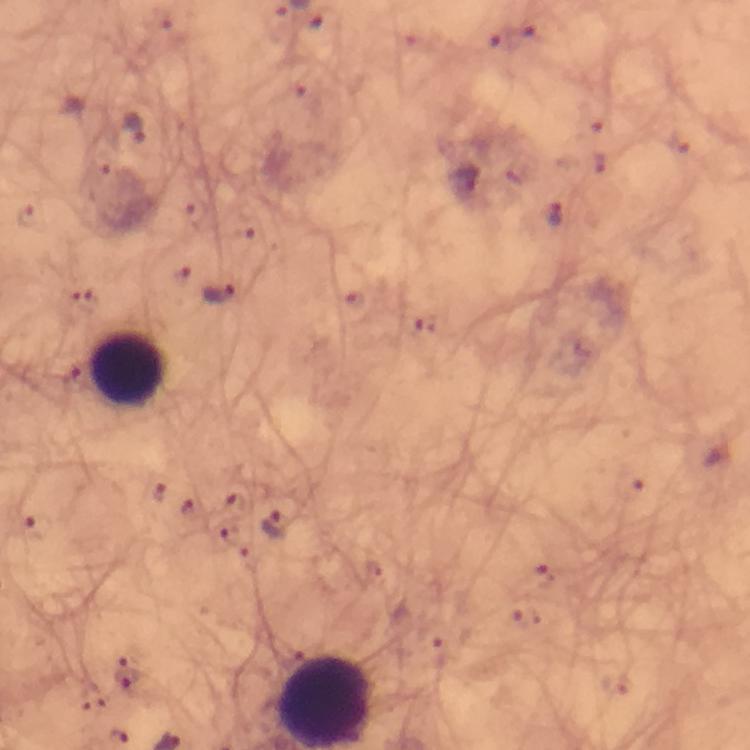

{
  "magnification": "100x",
  "stain": "Giemsa",
  "context": "from a diagnostic examination for malaria",
  "image_size": "750×750 pixels",
  "immersion_oil": "applied",
  "plasmodium_parasite_locations": "approximate centers as {x, y} in pixels: {133, 127}, {463, 180}, {556, 215}, {218, 292}, {274, 525}, {129, 675}",
  "preparation": "thick blood smear",
  "capture": "smartphone mounted on the microscope",
  "leukocyte_locations": "approximate centers as {x, y} in pixels: {128, 369}",
  "cropped_from": "a single field of view"
}